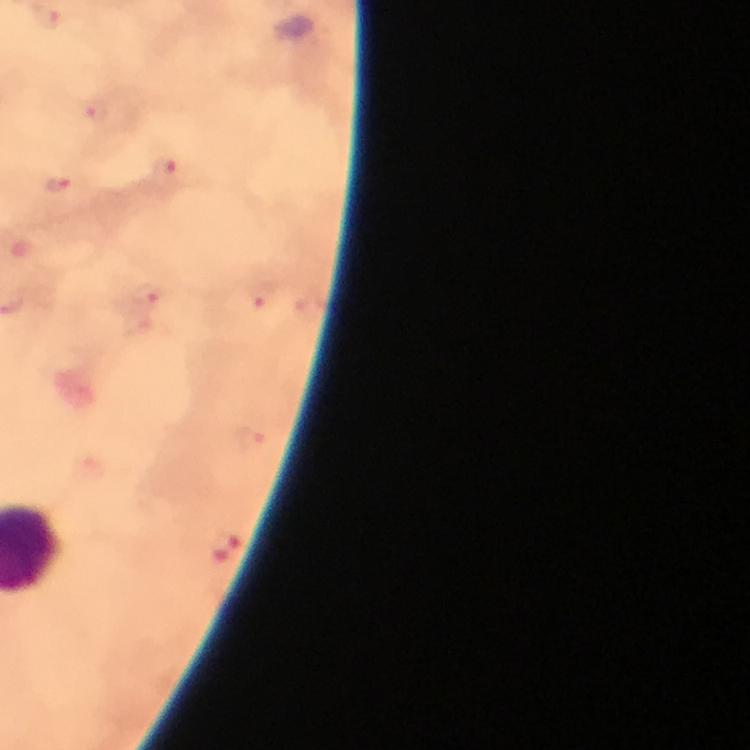
Approximate centers as [x, y] in pixels.
Summary:
  - Malaria parasite locations: [95, 109], [167, 169], [57, 185], [146, 293], [261, 295], [250, 440], [223, 547]
  - Stain: Giemsa
  - Magnification: 100x
  - Context: from a malaria diagnostic workup
  - Image size: 750×750 pixels
  - Cropped from: a single field of view
  - Capture: smartphone photograph through a microscope
  - Immersion oil: used
  - Preparation: thick blood smear